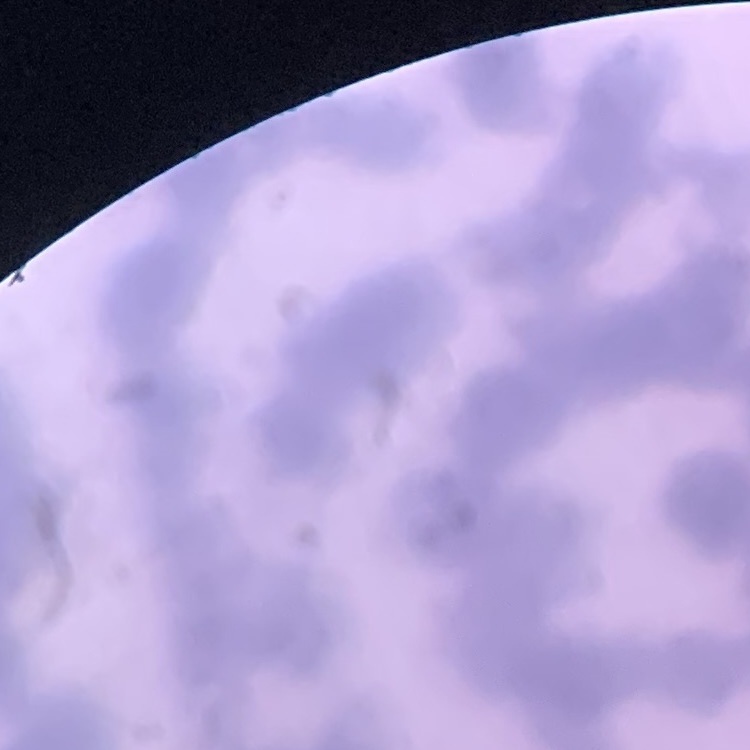

Summary:
  - Erythrocyte morphology: rouleaux formation
  - Stain: Field's or Giemsa
  - Preparation: thin blood smear
  - Image type: square crop of a larger photomicrograph